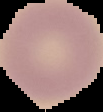
From a thin blood film. The area outside the segmented cell region is set to black. Image is 103×112 pixels. Result: negative for Plasmodium parasites.